Locate Plasmodium parasites and leukocytes.
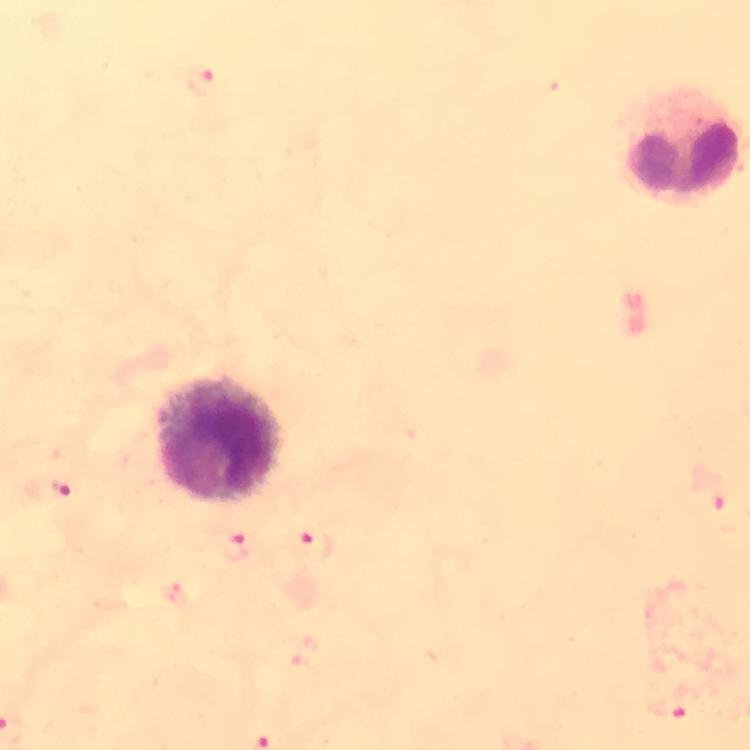

Approximate object centers, in pixels from the top-left corner.
Plasmodium parasites: (x=202, y=78), (x=58, y=486), (x=713, y=489), (x=314, y=543), (x=237, y=546), (x=669, y=707).
Leukocytes: (x=220, y=439).

Giemsa stain. Image is 750×750 pixels. Cropped region of a single field of view. Smartphone photograph taken through a microscope. Immersion oil was used. Thick blood smear. At 100x magnification. From a diagnostic examination for malaria.